Locate every blood parasite and identify its species.
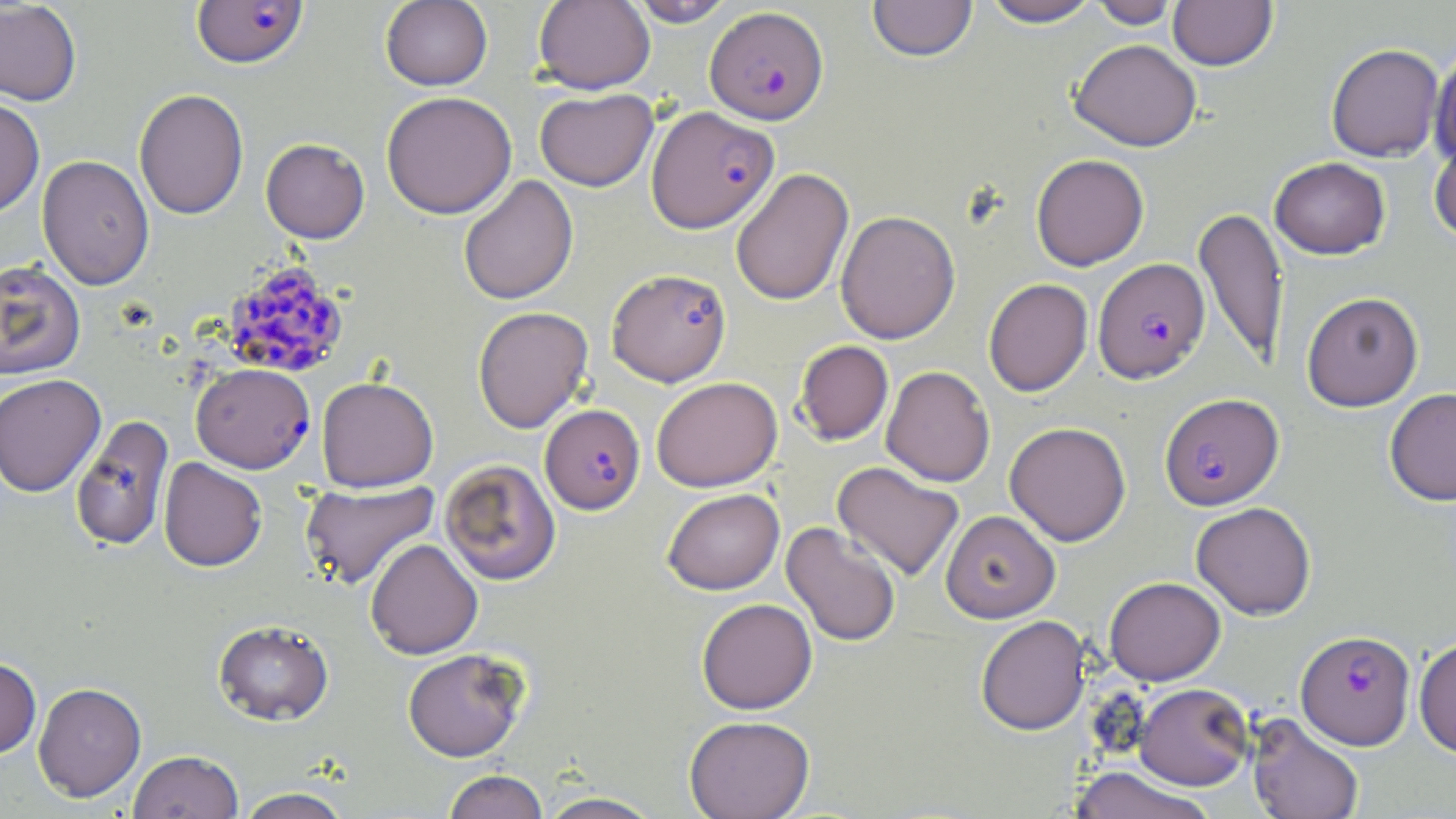
Approximate bounding boxes as (x1, y1, x2, y2) in pixels.
Plasmodium falciparum-infected red blood cells: (191, 1, 308, 69), (705, 6, 829, 124), (646, 105, 779, 233), (1093, 257, 1210, 383), (222, 258, 349, 379), (607, 268, 731, 386), (191, 363, 315, 473), (1160, 393, 1283, 510), (540, 404, 645, 514), (1295, 630, 1415, 749).
No Plasmodium ovale, Plasmodium malariae, Plasmodium vivax, Babesia divergens, or Trypanosoma brucei observed.

slide-level diagnosis = Plasmodium falciparum
stain = May-Grünwald-Giemsa
preparation = thin blood smear
uninfected red blood cell locations = approximate bounding boxes as (x1, y1, x2, y2) in pixels: (533, 0, 655, 95), (627, 0, 736, 27), (868, 0, 978, 62), (980, 0, 1103, 27), (1088, 0, 1181, 29), (1168, 0, 1278, 70), (0, 1, 82, 106), (380, 1, 493, 91), (1070, 39, 1202, 151), (1326, 43, 1444, 162), (1430, 43, 1456, 166), (134, 88, 249, 220), (535, 88, 658, 191), (381, 91, 517, 219), (0, 97, 45, 218), (1429, 134, 1456, 244), (261, 138, 370, 243), (1031, 154, 1149, 271), (37, 155, 155, 290), (1269, 157, 1390, 259), (731, 168, 854, 306), (458, 175, 578, 305), (1194, 206, 1289, 367), (835, 210, 960, 344), (0, 260, 86, 380), (983, 278, 1093, 397), (1301, 292, 1423, 411), (472, 306, 594, 433), (794, 340, 894, 445), (881, 366, 995, 486), (0, 373, 106, 498), (316, 376, 438, 491), (651, 376, 782, 492), (1384, 388, 1456, 506), (70, 414, 175, 553), (1004, 421, 1131, 546), (158, 458, 267, 572), (439, 458, 561, 585), (832, 461, 964, 581), (300, 480, 440, 590), (662, 488, 784, 595), (1190, 502, 1316, 619), (941, 510, 1060, 622), (781, 521, 901, 647), (365, 539, 483, 659), (1104, 577, 1226, 685), (696, 598, 817, 714), (975, 615, 1090, 735), (213, 619, 334, 726), (1414, 636, 1456, 757), (402, 648, 530, 762), (0, 656, 42, 758), (33, 682, 146, 801), (1134, 683, 1254, 790), (1247, 713, 1365, 819), (684, 715, 816, 819), (128, 750, 244, 819), (1069, 766, 1216, 819), (442, 769, 548, 819), (235, 787, 353, 818), (537, 791, 665, 818)
modality = light microscopy
image size = 1456×819 pixels
magnification = 1000x
field of view = one of a larger specimen